Assess this cell for malaria.
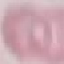
Uninfected.

stain = Giemsa
capture = smartphone camera at the microscope eyepiece
preparation = thin blood film
image type = automatically extracted cell patch, resized to 64 × 64 pixels